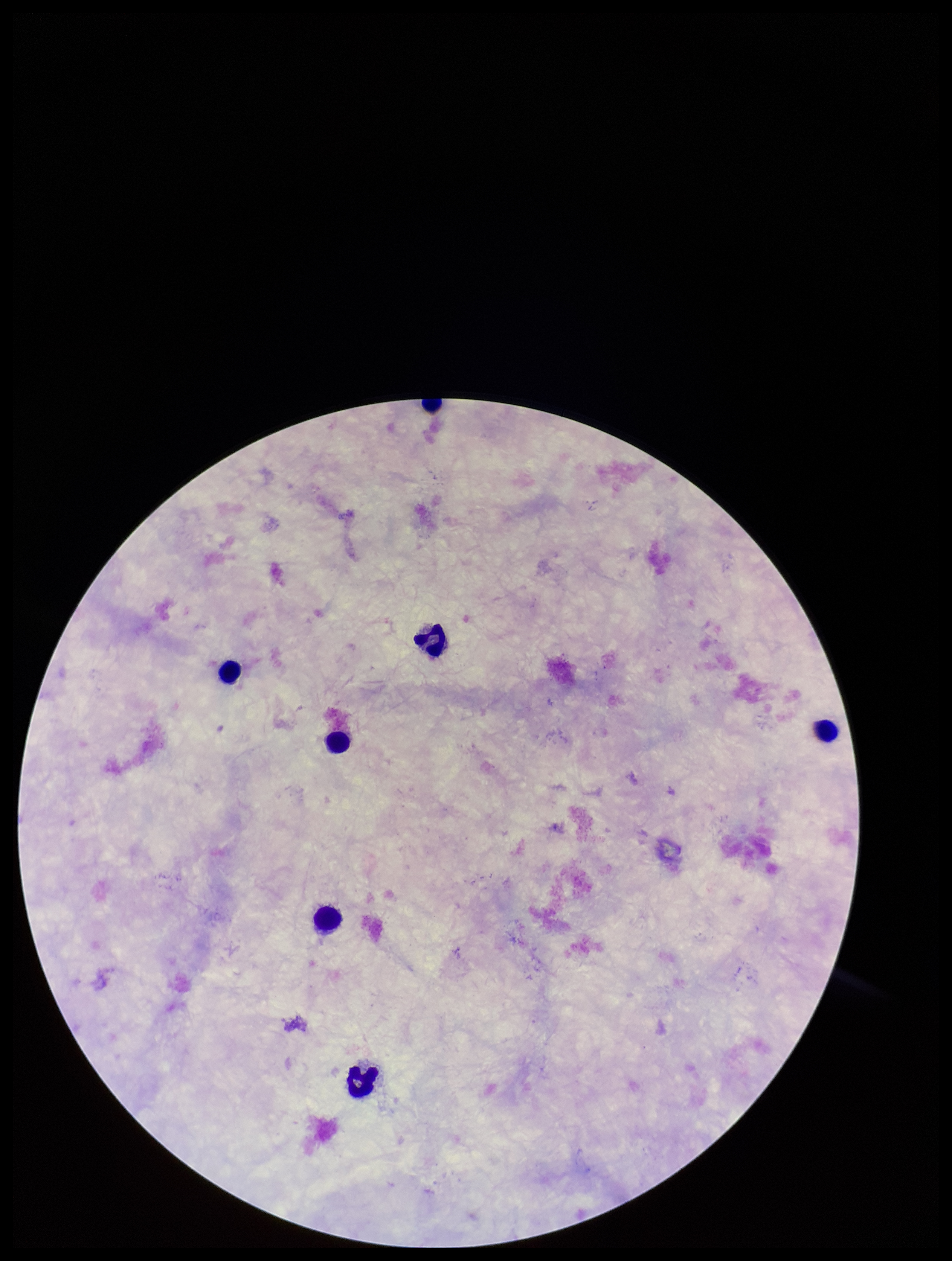 Preparation: thick blood smear. Parasite count: 0. One field from this slide. Stained with Giemsa. Plasmodium parasites: none seen. Leukocyte count: 7. Image is 952×1261 pixels. Smartphone photograph taken through the eyepiece of a microscope. Patient malaria status: negative.